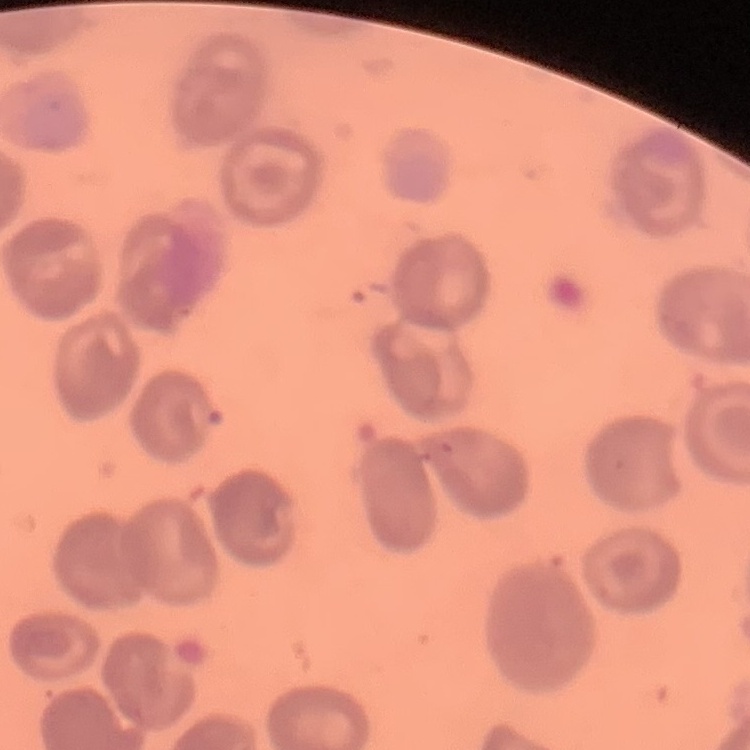

The erythrocytes exhibit no rouleaux formation. Stained with either Field's or Giemsa. Square crop of a larger photomicrograph. Thin blood film.